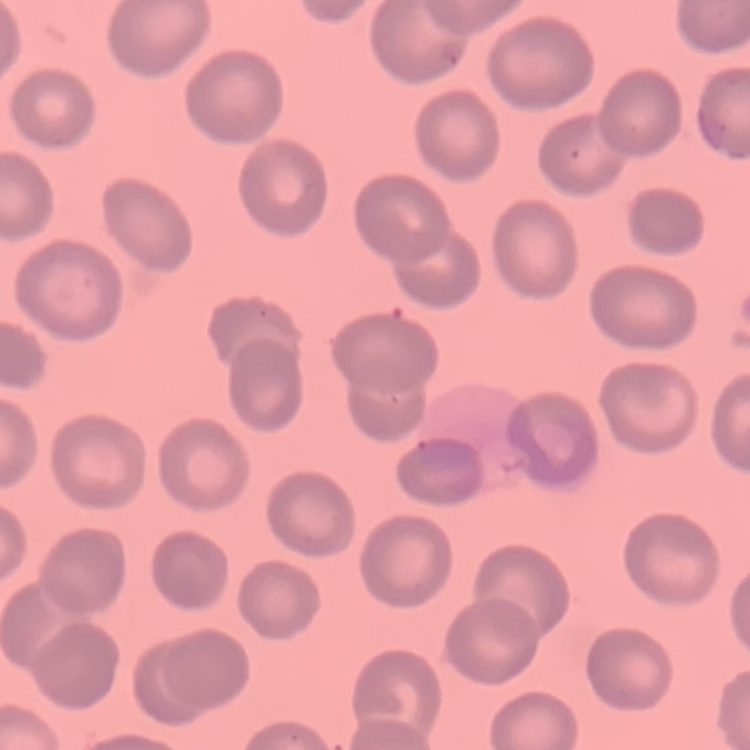 The red blood cells show no rouleaux formation. Thin blood smear. Square crop of a larger photomicrograph. Field's or Giemsa stain.